Report the malaria status of this cell.
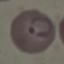
It is parasitized.

stain: Giemsa
capture: smartphone through the microscope eyepiece
image_type: automatically extracted cell patch, resized to 64 × 64 pixels
preparation: thin smear